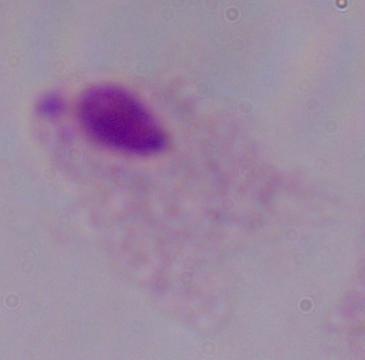

identification = trichomonad
magnification = 1000x
modality = micrograph